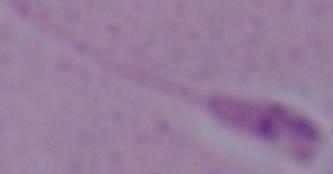

Summary:
  - Modality: photomicrograph
  - Identification: Leishmania
  - Magnification: 1000x